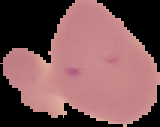

Summary:
  - Result: negative for malaria parasites
  - Preparation: thin blood film
  - Image size: 160×127 pixels
  - Image type: segmented cell region on a black background